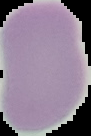
image size = 91×136 pixels
preparation = thin blood film
malaria status = uninfected
image type = cell region segmented out of the field of view; surrounding area masked to black